Mark where leukocytes are.
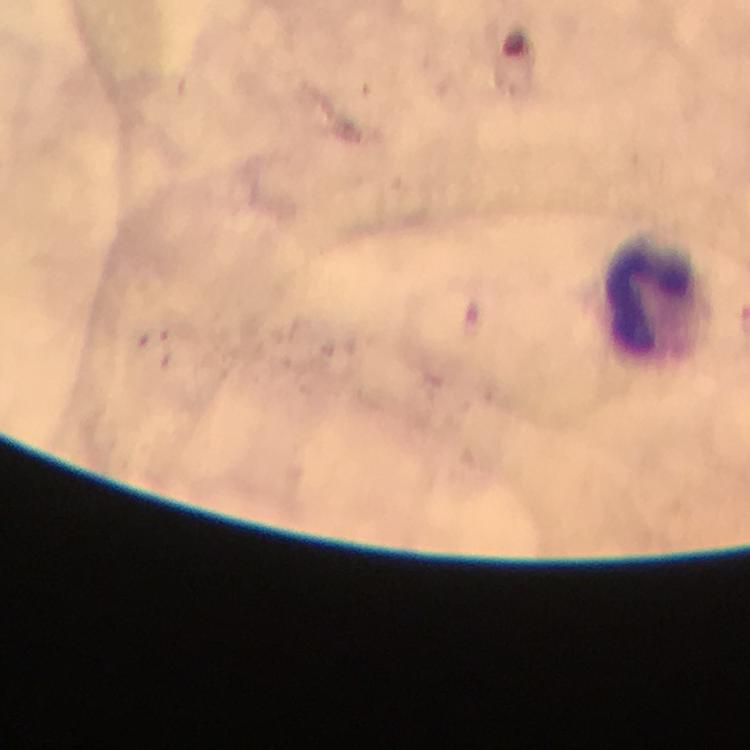

Approximate centers as {x, y} in pixels.
Leukocytes: {651, 298}.

magnification = 100x
cropped from = one field of view
image size = 750×750 pixels
immersion oil = applied
stain = Giemsa
preparation = thick blood film
capture = smartphone camera through the microscope
Plasmodium parasites = none seen
context = from a malaria diagnostic workup